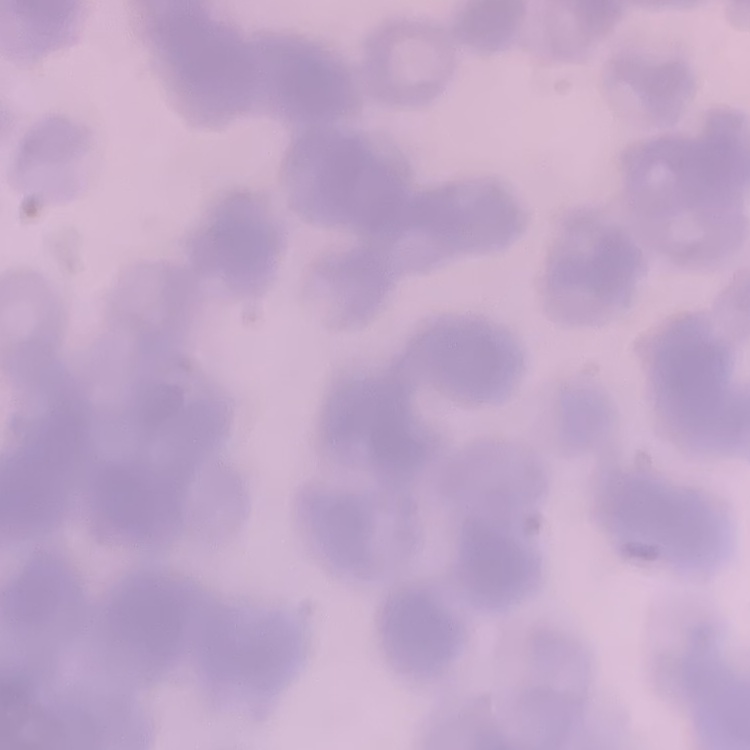

Summary:
  - Red blood cell morphology: rouleaux formation
  - Stain: Field's or Giemsa
  - Preparation: thin blood film
  - Image type: square crop of a larger photomicrograph